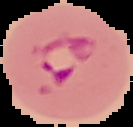

Image is 133×127 pixels. From a thin blood smear. Cell region segmented out of the field of view; the surrounding area is masked to black. Result: malaria parasites identified.